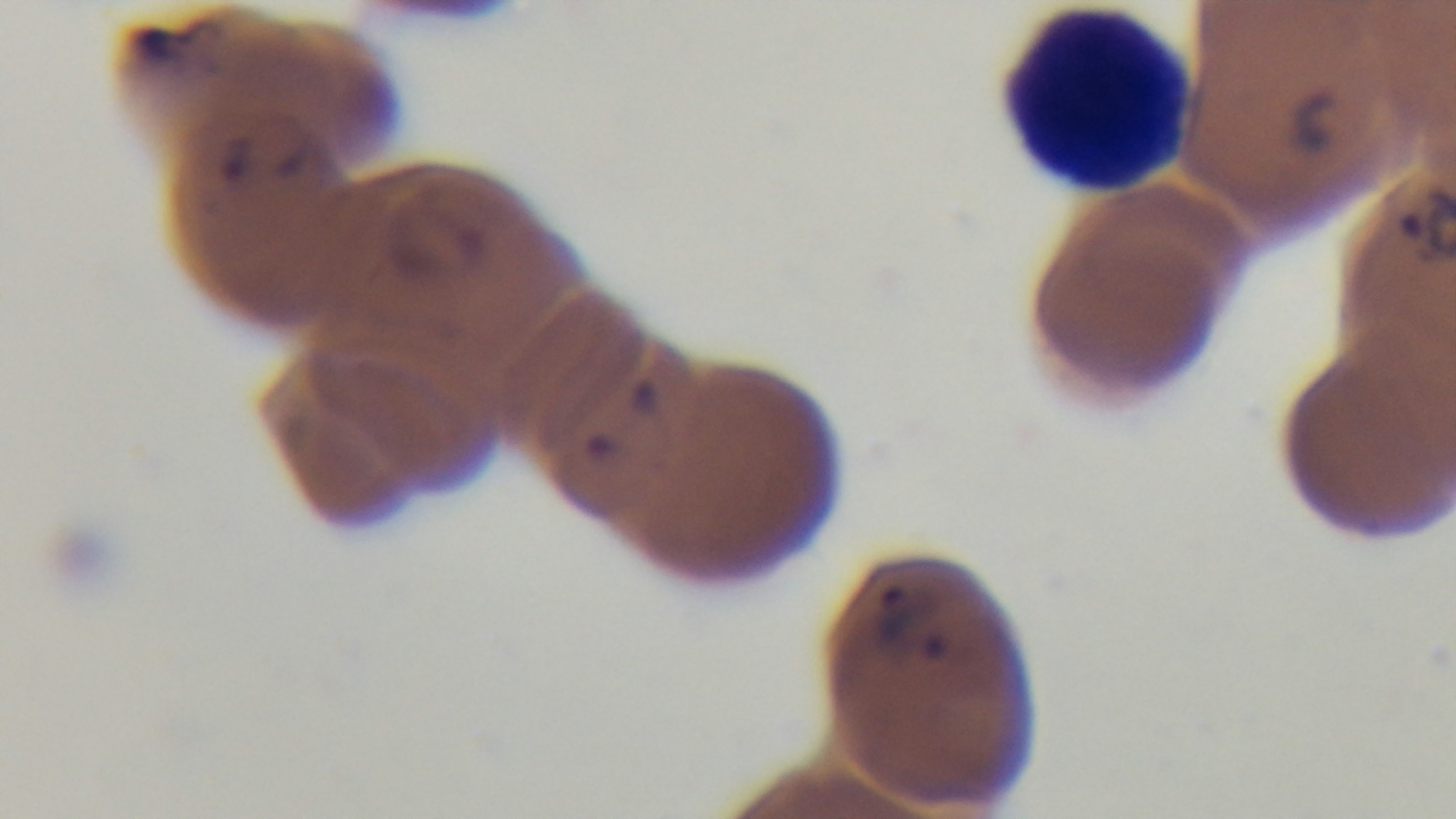
Summary:
  - Preparation: thin blood film
  - Field of view: single
  - Malaria status: positive
  - Stain: Giemsa
  - Modality: light microscopy
  - Capture: mounted 4K digital camera
  - Objective: 100x oil immersion